Outline each blood parasite and name the species.
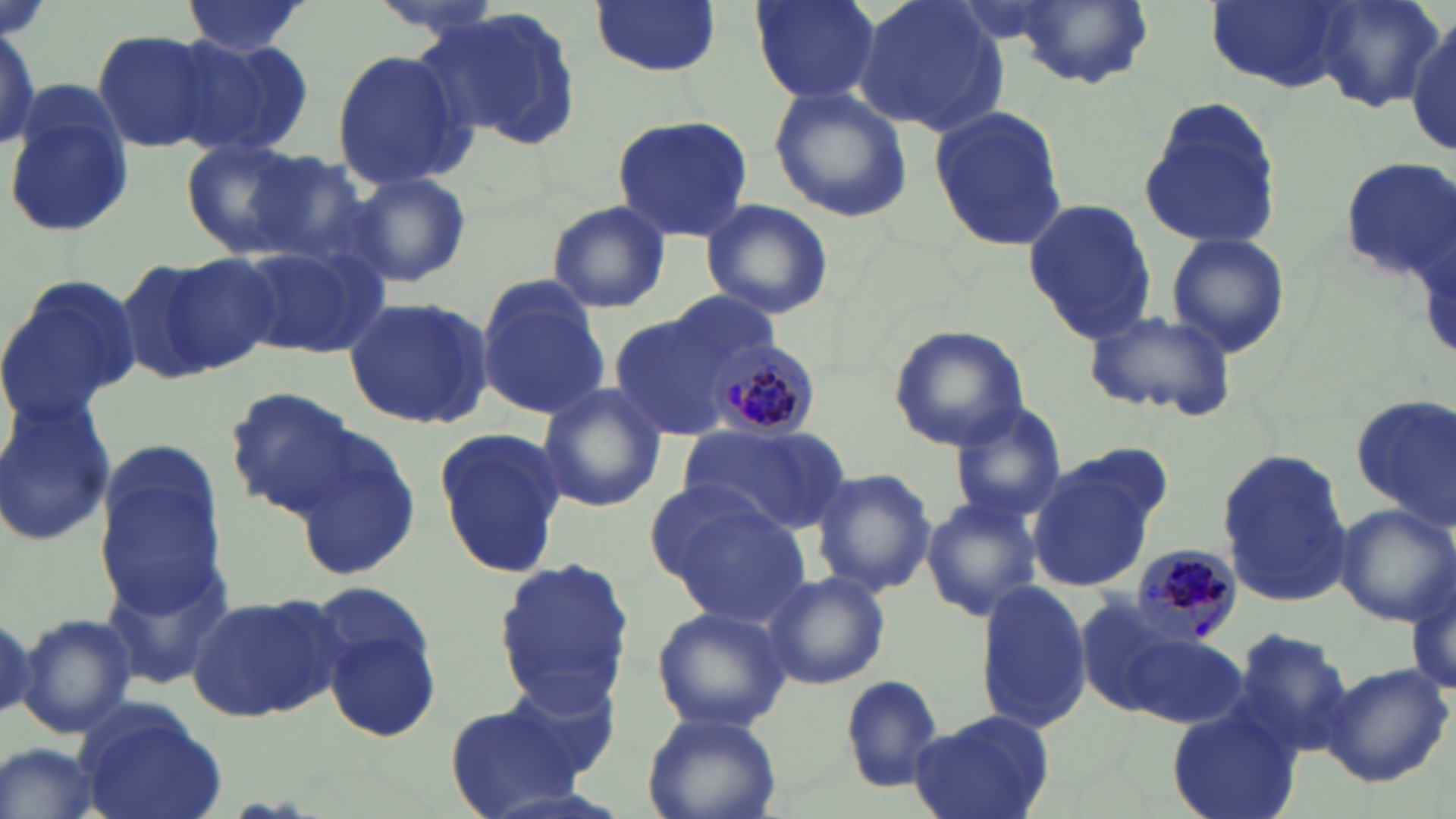
Approximate bounding boxes as (x1,y1)-(x2,y2) corner pairs in pixels.
Plasmodium malariae-infected red blood cells: (703,338)-(819,437), (1129,543)-(1244,651).
No Plasmodium falciparum, Plasmodium ovale, Plasmodium vivax, Babesia divergens, or Trypanosoma brucei observed.

{
  "slide_level_diagnosis": "Plasmodium malariae",
  "image_size": "1456×819 pixels",
  "preparation": "thin blood smear",
  "field_of_view": "one of a larger specimen",
  "stain": "May-Grünwald-Giemsa",
  "modality": "light microscopy",
  "magnification": "1000x",
  "uninfected_red_blood_cell_locations": "approximate bounding boxes as (x1,y1)-(x2,y2) corner pairs in pixels: (365,0)-(511,36), (748,0)-(882,103), (851,0)-(1010,138), (1207,0)-(1356,93), (181,1)-(310,56), (591,1)-(721,77), (1009,1)-(1156,90), (1308,1)-(1444,113), (428,8)-(585,150), (1408,19)-(1456,157), (1,20)-(42,154), (91,28)-(221,153), (173,33)-(315,160), (331,47)-(471,189), (767,84)-(914,223), (5,86)-(138,240), (1137,97)-(1280,251), (928,105)-(1066,253), (611,113)-(756,246), (182,140)-(308,257), (240,150)-(375,268), (1335,157)-(1456,279), (345,171)-(472,288), (699,198)-(834,320), (1022,198)-(1158,344), (545,199)-(671,313), (1165,232)-(1291,359), (237,242)-(386,360), (159,250)-(284,375), (114,257)-(233,386), (0,273)-(142,430), (476,278)-(611,419), (663,292)-(783,382), (343,296)-(493,431), (1084,308)-(1240,420), (608,313)-(738,439), (888,324)-(1029,451), (537,381)-(665,513), (225,386)-(365,517), (1351,389)-(1455,525), (0,396)-(117,548), (947,402)-(1065,521), (684,424)-(852,537), (432,425)-(568,578), (290,433)-(420,584), (90,445)-(226,616), (1215,447)-(1354,608), (1024,457)-(1159,590), (810,466)-(938,596), (921,495)-(1042,624), (665,501)-(809,626), (1331,502)-(1455,626), (102,555)-(233,692), (494,557)-(631,709), (1406,567)-(1455,704), (764,571)-(889,690), (974,582)-(1093,733), (186,592)-(343,722), (1072,595)-(1195,715), (317,599)-(442,744), (651,605)-(790,733), (16,612)-(138,739), (1232,625)-(1356,756), (1112,626)-(1248,732), (1320,661)-(1452,787), (503,664)-(623,784), (839,674)-(948,794), (444,699)-(592,817), (74,701)-(227,819), (1166,705)-(1300,819), (908,709)-(1058,819), (642,710)-(782,819), (0,741)-(104,819)"
}